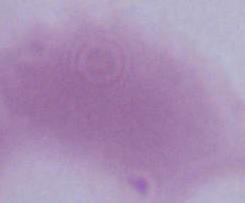 1000x magnification. An erythrocyte is shown. Micrograph.